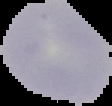
Summary:
  - Image size: 112×106 pixels
  - Image type: segmented cell region with the area outside set to black
  - Preparation: thin blood smear
  - Malaria status: uninfected